Comment on the morphology of the erythrocytes.
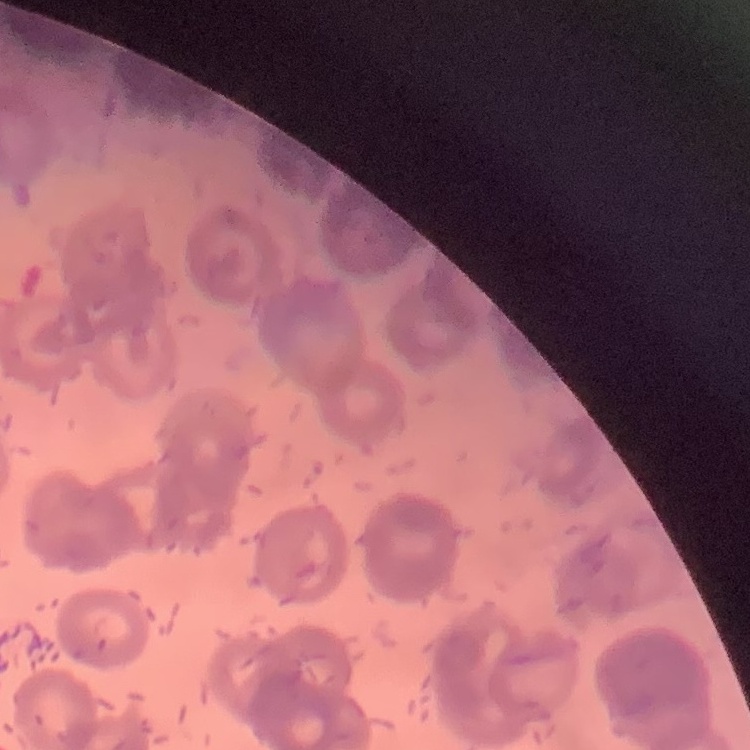

Rouleaux formation.

Thin peripheral smear. One tile cut from a larger photomicrograph. Field's or Giemsa stain.